Locate every malaria parasite.
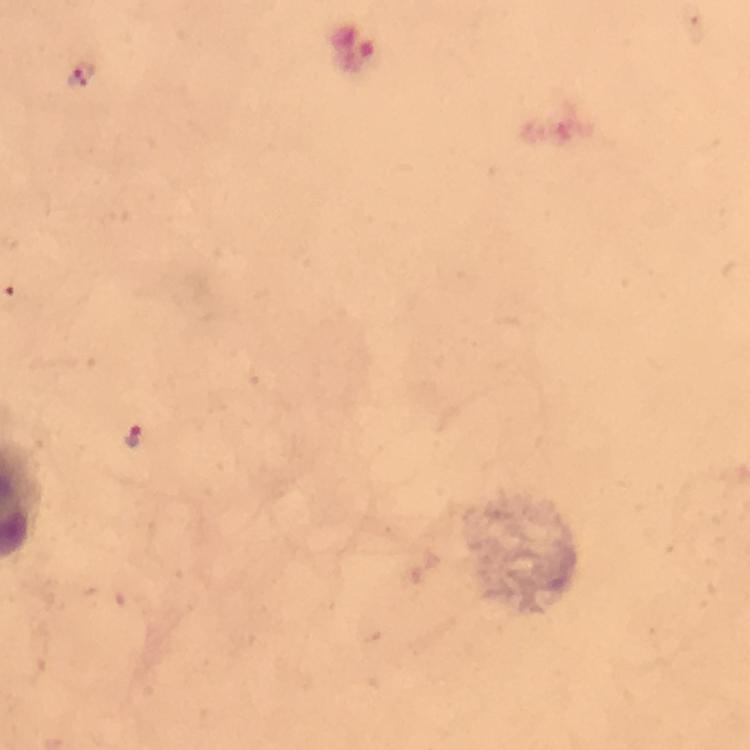
Approximate object centers, in pixels from the top-left corner.
Malaria parasites: (x=81, y=74), (x=133, y=436).

cropped from = one field of view
context = from a malaria diagnostic workup
image size = 750×750 pixels
immersion oil = used
preparation = thick smear
stain = Giemsa
magnification = 100x
capture = smartphone photograph through a microscope